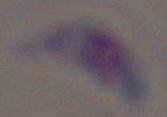
identification: Toxoplasma gondii
modality: photomicrograph
magnification: 1000x